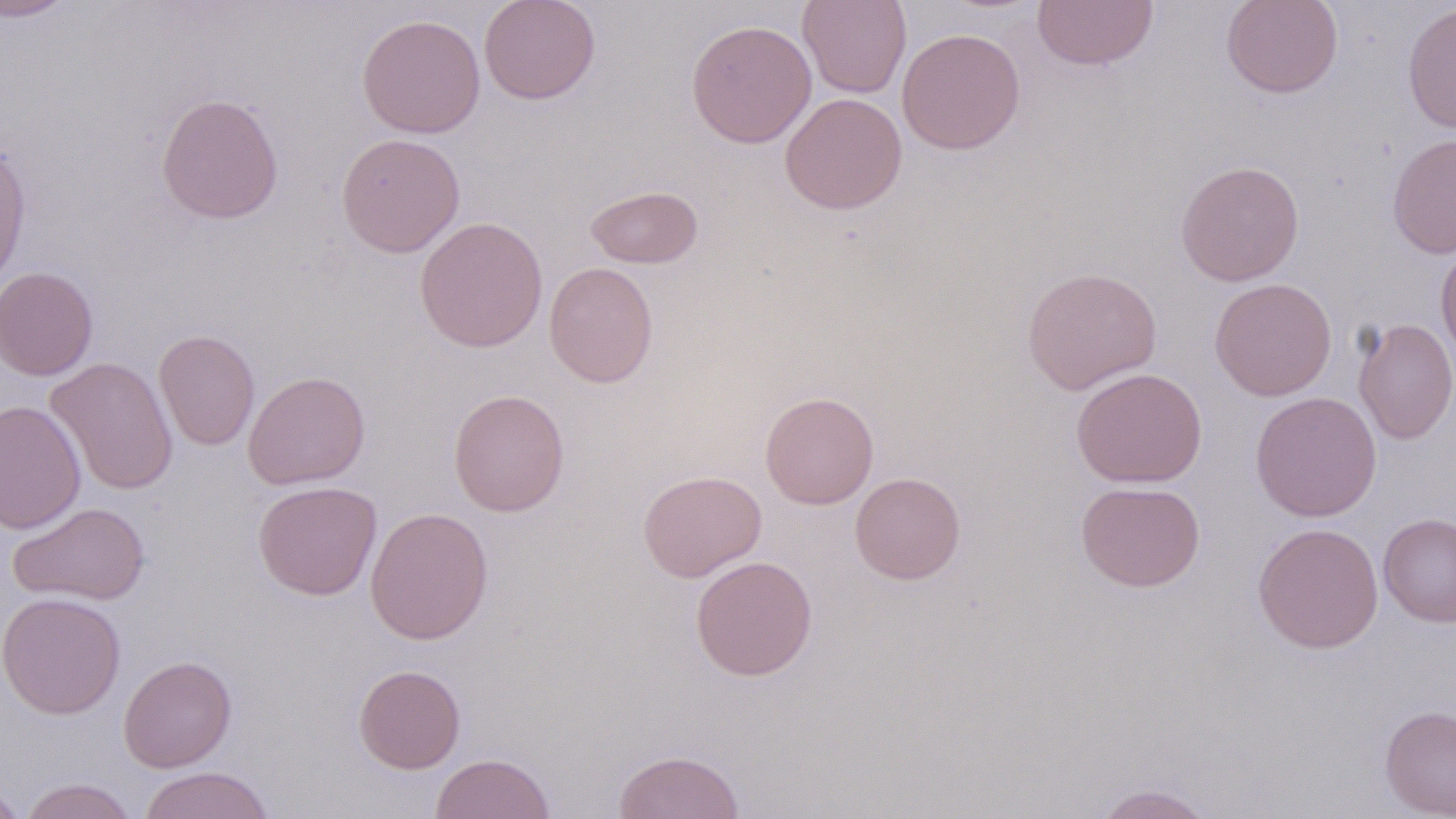

Summary:
  - Coordinate format: approximate bounding boxes as named x1/y1/x2/y2 corners in pixels
  - Uninfected red blood cell locations: (x1=0, y1=0, x2=77, y2=22), (x1=479, y1=0, x2=601, y2=105), (x1=797, y1=0, x2=911, y2=98), (x1=1031, y1=0, x2=1159, y2=71), (x1=1220, y1=0, x2=1343, y2=98), (x1=1402, y1=3, x2=1456, y2=134), (x1=356, y1=13, x2=485, y2=139), (x1=687, y1=19, x2=816, y2=148), (x1=896, y1=27, x2=1026, y2=155), (x1=156, y1=93, x2=284, y2=224), (x1=780, y1=93, x2=907, y2=214), (x1=1387, y1=132, x2=1456, y2=259), (x1=336, y1=133, x2=465, y2=257), (x1=0, y1=143, x2=32, y2=290), (x1=1175, y1=160, x2=1304, y2=287), (x1=585, y1=185, x2=703, y2=269), (x1=414, y1=216, x2=548, y2=353), (x1=1436, y1=243, x2=1456, y2=362), (x1=544, y1=261, x2=659, y2=388), (x1=0, y1=266, x2=98, y2=380), (x1=1021, y1=266, x2=1162, y2=395), (x1=1210, y1=278, x2=1337, y2=401), (x1=1353, y1=317, x2=1456, y2=445), (x1=154, y1=329, x2=260, y2=451), (x1=44, y1=357, x2=179, y2=495), (x1=1071, y1=367, x2=1208, y2=488), (x1=242, y1=370, x2=371, y2=489), (x1=448, y1=389, x2=570, y2=516), (x1=759, y1=391, x2=878, y2=509), (x1=1249, y1=391, x2=1382, y2=522), (x1=0, y1=399, x2=87, y2=535), (x1=638, y1=469, x2=767, y2=583), (x1=850, y1=472, x2=966, y2=584), (x1=252, y1=480, x2=381, y2=600), (x1=1075, y1=480, x2=1205, y2=592), (x1=7, y1=502, x2=151, y2=606), (x1=365, y1=506, x2=494, y2=644), (x1=1377, y1=513, x2=1456, y2=627), (x1=1252, y1=522, x2=1384, y2=653), (x1=690, y1=555, x2=818, y2=681), (x1=0, y1=591, x2=126, y2=719), (x1=118, y1=654, x2=237, y2=772), (x1=353, y1=664, x2=466, y2=773), (x1=1380, y1=704, x2=1456, y2=818), (x1=613, y1=749, x2=744, y2=819), (x1=430, y1=752, x2=556, y2=818), (x1=137, y1=766, x2=275, y2=819), (x1=0, y1=777, x2=26, y2=818), (x1=19, y1=778, x2=139, y2=819), (x1=1093, y1=783, x2=1217, y2=819)
  - Slide-level diagnosis: negative for blood parasites
  - Preparation: thin blood smear
  - Stain: May-Grünwald-Giemsa
  - Image size: 1456×819 pixels
  - Magnification: 1000x
  - Field of view: single
  - Modality: optical microscopy